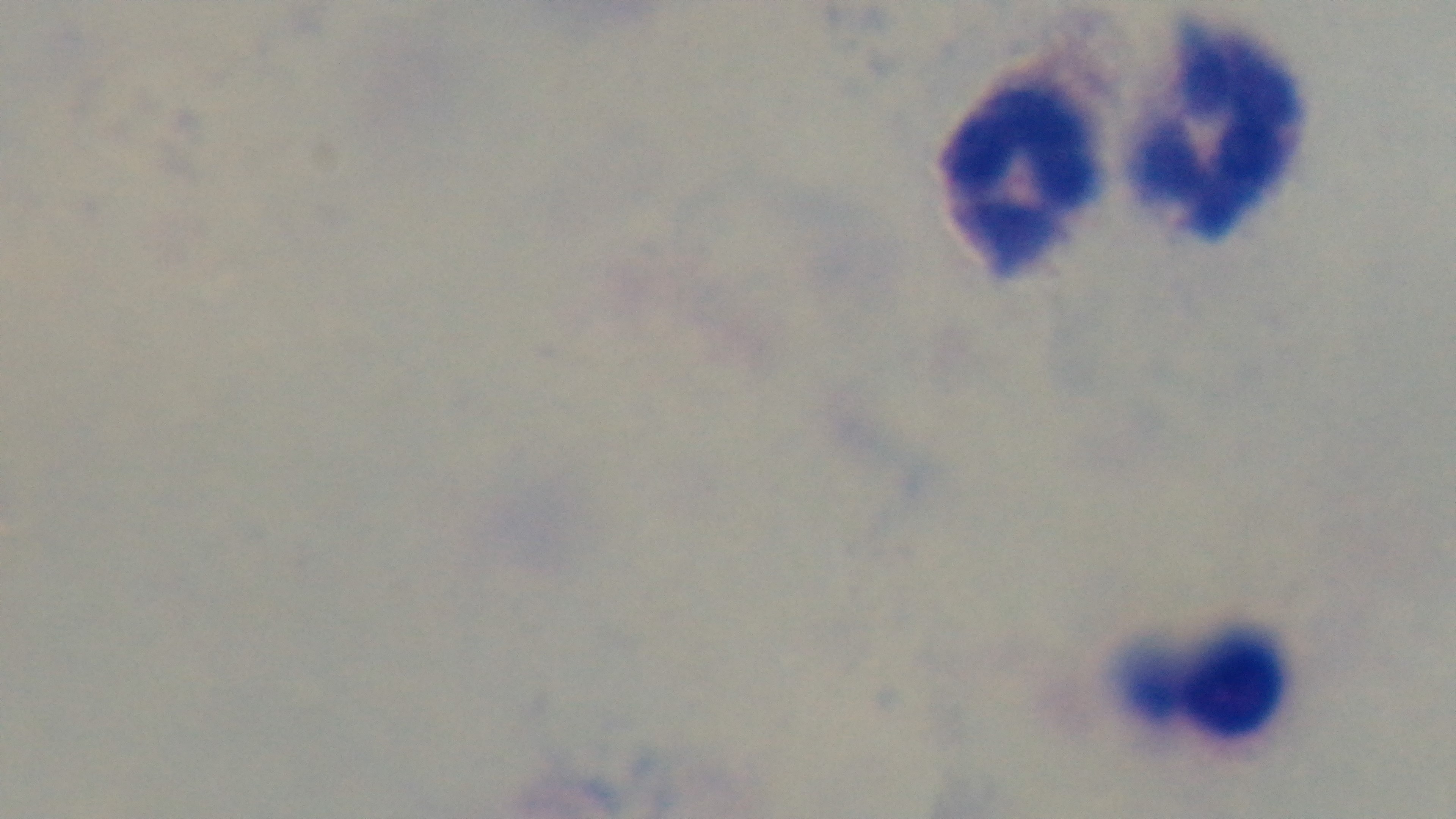
stain: Giemsa
preparation: thick smear
capture: mounted 4K digital camera
field_of_view: one from the slide
objective: 100x oil immersion
modality: light microscopy
malaria_status: uninfected